Locate every leukocyte (white blood cell).
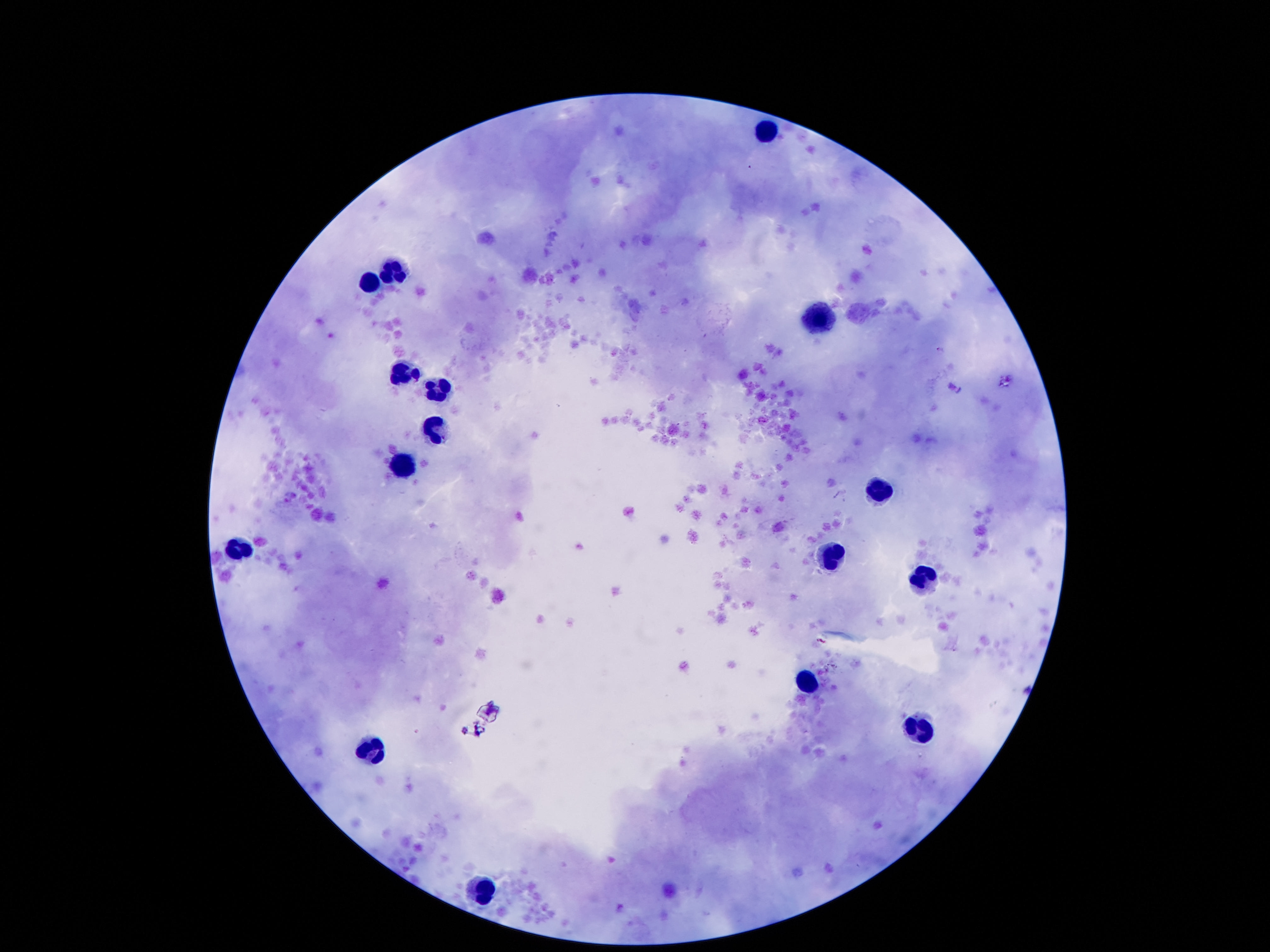

Approximate centers as {x, y} in pixels.
Leukocytes: {767, 132}, {395, 268}, {373, 281}, {815, 320}, {398, 365}, {437, 391}, {431, 429}, {402, 462}, {880, 488}, {243, 549}, {828, 555}, {922, 581}, {812, 678}, {915, 730}, {376, 749}, {482, 888}.

magnification = 100x
capture = smartphone camera through the microscope eyepiece
field of view = one from this slide
image size = 1270×952 pixels
preparation = thick blood film
patient malaria status = negative
stain = Giemsa